Outline each uninfected red blood cell.
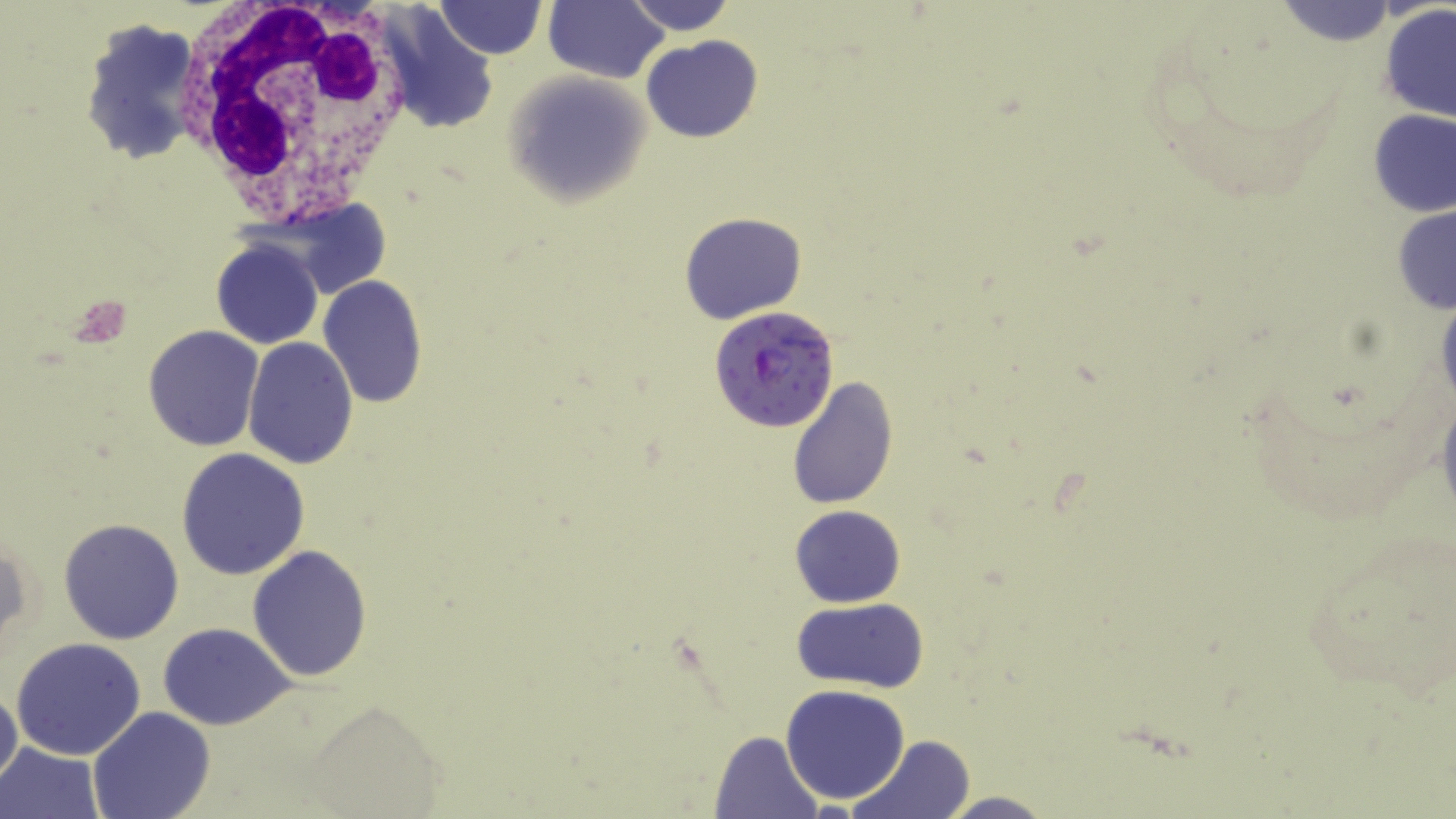
Approximate bounding boxes as named x1/y1/x2/y2 corners in pixels.
Uninfected red blood cells: (x1=437, y1=0, x2=544, y2=59), (x1=544, y1=0, x2=669, y2=84), (x1=624, y1=0, x2=736, y2=36), (x1=1273, y1=2, x2=1404, y2=49), (x1=379, y1=6, x2=500, y2=138), (x1=1380, y1=6, x2=1456, y2=125), (x1=78, y1=15, x2=205, y2=164), (x1=641, y1=36, x2=763, y2=142), (x1=503, y1=72, x2=648, y2=208), (x1=1366, y1=107, x2=1455, y2=218), (x1=280, y1=199, x2=393, y2=300), (x1=1393, y1=201, x2=1456, y2=317), (x1=680, y1=211, x2=807, y2=326), (x1=212, y1=237, x2=323, y2=349), (x1=317, y1=275, x2=426, y2=409), (x1=1433, y1=279, x2=1456, y2=421), (x1=142, y1=326, x2=264, y2=450), (x1=241, y1=338, x2=359, y2=468), (x1=789, y1=375, x2=898, y2=508), (x1=1435, y1=389, x2=1456, y2=528), (x1=176, y1=447, x2=309, y2=581), (x1=790, y1=504, x2=907, y2=608), (x1=1297, y1=515, x2=1456, y2=710), (x1=59, y1=518, x2=184, y2=645), (x1=2, y1=535, x2=32, y2=655), (x1=248, y1=545, x2=375, y2=683), (x1=791, y1=595, x2=929, y2=693), (x1=157, y1=624, x2=298, y2=729), (x1=11, y1=637, x2=147, y2=760), (x1=780, y1=684, x2=911, y2=804), (x1=0, y1=685, x2=23, y2=792), (x1=304, y1=706, x2=445, y2=813), (x1=87, y1=707, x2=217, y2=819), (x1=708, y1=731, x2=824, y2=816), (x1=852, y1=734, x2=974, y2=819), (x1=0, y1=742, x2=104, y2=819), (x1=934, y1=791, x2=1055, y2=818).

Summary:
  - White blood cell locations: (x1=178, y1=0, x2=420, y2=225)
  - Plasmodium falciparum-infected red blood cell locations: (x1=709, y1=305, x2=839, y2=432)
  - Slide-level diagnosis: Plasmodium falciparum
  - Field of view: single
  - Modality: light microscopy
  - Magnification: 1000x
  - Stain: May-Grünwald-Giemsa
  - Preparation: thin blood film
  - Image size: 1456×819 pixels